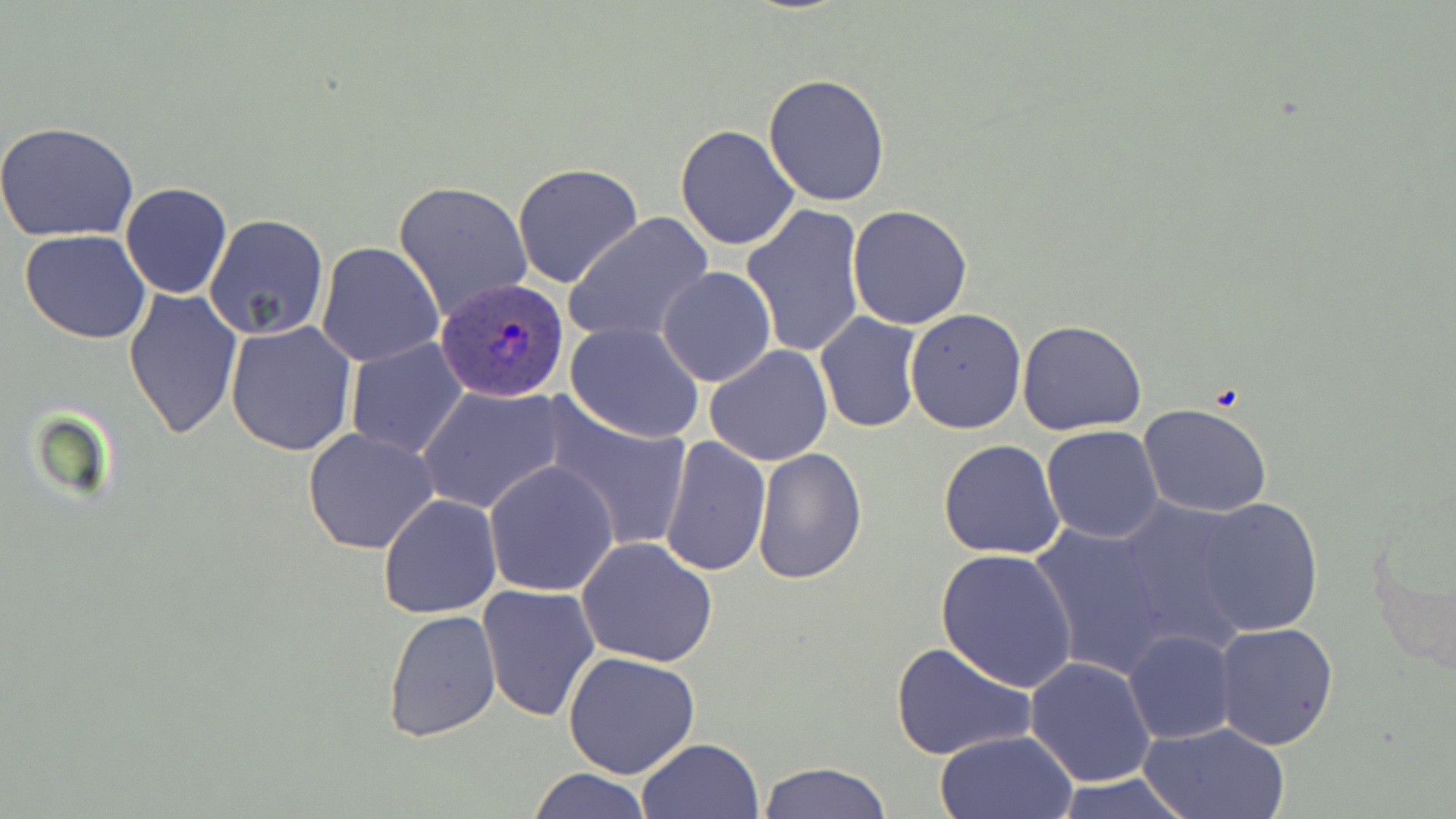
{
  "slide_level_diagnosis": "Plasmodium ovale",
  "preparation": "thin blood film",
  "plasmodium_ovale_infected_red_blood_cell_locations": "approximate bounding boxes as (x1,y1)-(x2,y2) corner pairs in pixels: (434,278)-(569,401)",
  "stain": "May-Grünwald-Giemsa",
  "magnification": "1000x",
  "field_of_view": "single",
  "modality": "light microscopy",
  "image_size": "1456×819 pixels",
  "uninfected_red_blood_cell_locations": "approximate bounding boxes as (x1,y1)-(x2,y2) corner pairs in pixels: (763,75)-(891,207), (0,124)-(140,243), (675,124)-(801,249), (511,162)-(644,289), (392,179)-(532,321), (120,182)-(233,299), (741,202)-(866,359), (846,204)-(974,330), (204,212)-(330,341), (562,212)-(714,346), (21,230)-(152,344), (315,241)-(445,368), (674,241)-(835,378), (657,267)-(775,388), (124,288)-(243,440), (905,309)-(1027,434), (815,310)-(923,434), (224,319)-(357,456), (1018,320)-(1147,436), (565,321)-(705,442), (344,337)-(470,461), (705,344)-(835,466), (417,385)-(564,514), (540,398)-(695,554), (1138,403)-(1274,518), (1041,425)-(1164,544), (301,429)-(442,554), (660,436)-(770,577), (938,438)-(1067,561), (752,446)-(868,584), (483,459)-(621,597), (1360,485)-(1456,675), (378,494)-(502,618), (1112,496)-(1258,652), (1191,498)-(1324,637), (1028,523)-(1173,677), (575,536)-(718,668), (934,547)-(1079,692), (477,584)-(601,721), (383,608)-(501,744), (1212,623)-(1341,751), (1123,630)-(1236,744), (890,639)-(1035,760), (563,650)-(699,779), (1024,657)-(1156,788), (1139,721)-(1291,819), (934,729)-(1077,818), (636,738)-(765,819), (758,761)-(892,819), (527,767)-(653,819), (1047,776)-(1197,819)"
}